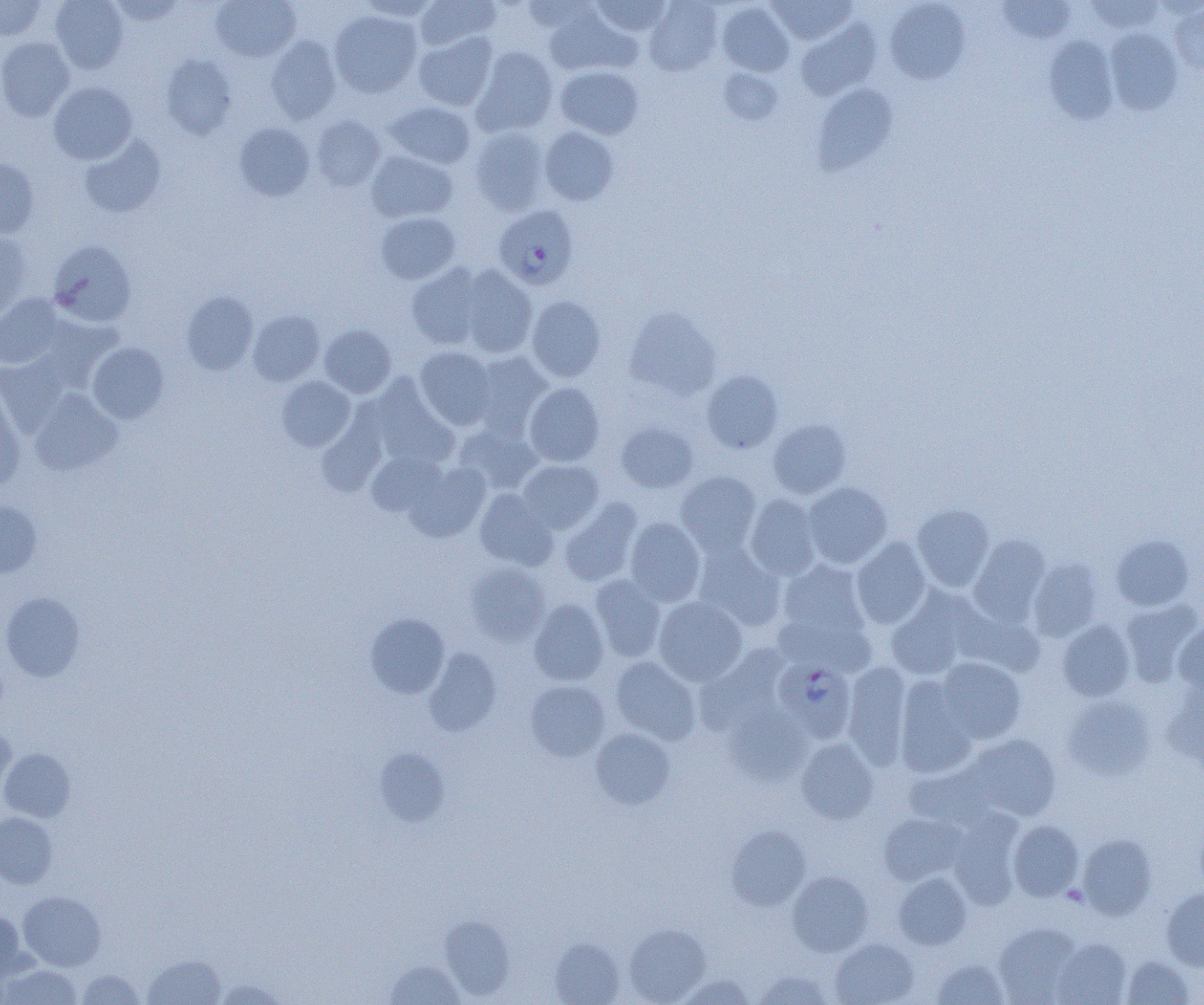

Approximate bounding boxes as named x1/y1/x2/y2 corners in pixels. Uninfected red blood cell locations: (x1=0, y1=0, x2=47, y2=40), (x1=50, y1=0, x2=128, y2=74), (x1=108, y1=0, x2=186, y2=26), (x1=210, y1=0, x2=302, y2=62), (x1=356, y1=0, x2=440, y2=22), (x1=415, y1=0, x2=500, y2=51), (x1=521, y1=0, x2=599, y2=34), (x1=590, y1=0, x2=672, y2=36), (x1=644, y1=0, x2=722, y2=75), (x1=768, y1=0, x2=857, y2=45), (x1=996, y1=0, x2=1077, y2=45), (x1=1082, y1=0, x2=1166, y2=34), (x1=885, y1=1, x2=969, y2=84), (x1=717, y1=2, x2=794, y2=77), (x1=1169, y1=3, x2=1204, y2=76), (x1=544, y1=7, x2=636, y2=76), (x1=329, y1=10, x2=422, y2=98), (x1=795, y1=19, x2=880, y2=101), (x1=1104, y1=28, x2=1183, y2=115), (x1=413, y1=32, x2=498, y2=111), (x1=266, y1=35, x2=342, y2=124), (x1=1044, y1=35, x2=1119, y2=124), (x1=0, y1=37, x2=75, y2=121), (x1=471, y1=47, x2=558, y2=136), (x1=159, y1=54, x2=237, y2=140), (x1=555, y1=66, x2=644, y2=139), (x1=718, y1=68, x2=783, y2=125), (x1=48, y1=82, x2=137, y2=164), (x1=810, y1=83, x2=900, y2=175), (x1=384, y1=102, x2=475, y2=169), (x1=311, y1=115, x2=387, y2=191), (x1=234, y1=122, x2=314, y2=201), (x1=469, y1=125, x2=551, y2=215), (x1=539, y1=126, x2=619, y2=206), (x1=79, y1=136, x2=166, y2=218), (x1=366, y1=151, x2=458, y2=222), (x1=0, y1=157, x2=40, y2=238), (x1=375, y1=211, x2=460, y2=285), (x1=0, y1=232, x2=33, y2=319), (x1=48, y1=239, x2=137, y2=327), (x1=407, y1=263, x2=487, y2=350), (x1=457, y1=265, x2=537, y2=358), (x1=181, y1=291, x2=258, y2=375), (x1=0, y1=294, x2=64, y2=369), (x1=526, y1=295, x2=606, y2=382), (x1=623, y1=307, x2=722, y2=401), (x1=247, y1=310, x2=325, y2=386), (x1=320, y1=325, x2=396, y2=398), (x1=87, y1=342, x2=169, y2=423), (x1=415, y1=347, x2=497, y2=430), (x1=471, y1=351, x2=553, y2=436), (x1=0, y1=354, x2=70, y2=436), (x1=701, y1=370, x2=783, y2=454), (x1=276, y1=376, x2=355, y2=451), (x1=368, y1=378, x2=459, y2=469), (x1=524, y1=382, x2=605, y2=466), (x1=0, y1=386, x2=24, y2=491), (x1=29, y1=389, x2=122, y2=476), (x1=316, y1=411, x2=387, y2=497), (x1=768, y1=419, x2=851, y2=498), (x1=616, y1=421, x2=697, y2=493), (x1=454, y1=424, x2=543, y2=495), (x1=366, y1=451, x2=447, y2=517), (x1=517, y1=459, x2=604, y2=534), (x1=405, y1=462, x2=490, y2=542), (x1=676, y1=471, x2=762, y2=557), (x1=802, y1=481, x2=892, y2=569), (x1=474, y1=488, x2=558, y2=571), (x1=745, y1=493, x2=822, y2=580), (x1=559, y1=497, x2=643, y2=587), (x1=0, y1=500, x2=42, y2=577), (x1=911, y1=504, x2=995, y2=592), (x1=625, y1=517, x2=705, y2=607), (x1=1110, y1=534, x2=1195, y2=611), (x1=968, y1=535, x2=1051, y2=624), (x1=851, y1=537, x2=932, y2=629), (x1=692, y1=542, x2=786, y2=631), (x1=1028, y1=557, x2=1103, y2=641), (x1=777, y1=559, x2=871, y2=645), (x1=464, y1=562, x2=552, y2=645), (x1=589, y1=574, x2=667, y2=662), (x1=886, y1=586, x2=981, y2=680), (x1=1, y1=591, x2=85, y2=681), (x1=654, y1=596, x2=747, y2=686), (x1=529, y1=598, x2=609, y2=686), (x1=1120, y1=599, x2=1202, y2=686), (x1=953, y1=602, x2=1044, y2=677), (x1=365, y1=613, x2=449, y2=698), (x1=1056, y1=619, x2=1136, y2=701), (x1=1173, y1=620, x2=1204, y2=696), (x1=696, y1=646, x2=793, y2=738), (x1=423, y1=648, x2=501, y2=737), (x1=610, y1=657, x2=701, y2=746), (x1=934, y1=657, x2=1027, y2=744), (x1=842, y1=662, x2=912, y2=769), (x1=894, y1=676, x2=980, y2=778), (x1=525, y1=680, x2=610, y2=762), (x1=1161, y1=684, x2=1204, y2=772), (x1=1061, y1=694, x2=1158, y2=781), (x1=722, y1=701, x2=811, y2=784), (x1=590, y1=727, x2=675, y2=810), (x1=0, y1=728, x2=16, y2=800), (x1=965, y1=734, x2=1061, y2=821), (x1=796, y1=737, x2=879, y2=824), (x1=375, y1=747, x2=450, y2=827), (x1=1, y1=748, x2=75, y2=821), (x1=904, y1=764, x2=999, y2=831), (x1=948, y1=810, x2=1025, y2=908), (x1=0, y1=812, x2=58, y2=888), (x1=878, y1=812, x2=967, y2=887), (x1=1008, y1=820, x2=1084, y2=901), (x1=726, y1=826, x2=811, y2=910), (x1=1077, y1=833, x2=1157, y2=920), (x1=787, y1=870, x2=873, y2=956), (x1=893, y1=872, x2=971, y2=949), (x1=1161, y1=887, x2=1204, y2=970), (x1=18, y1=890, x2=106, y2=971), (x1=0, y1=910, x2=28, y2=980), (x1=440, y1=916, x2=515, y2=1000), (x1=993, y1=922, x2=1084, y2=1004), (x1=623, y1=924, x2=711, y2=1004), (x1=1052, y1=937, x2=1132, y2=1005), (x1=549, y1=938, x2=624, y2=1005), (x1=830, y1=938, x2=918, y2=1005), (x1=143, y1=954, x2=226, y2=1004), (x1=1122, y1=955, x2=1195, y2=1005), (x1=932, y1=957, x2=1009, y2=1005), (x1=386, y1=959, x2=464, y2=1004), (x1=1, y1=963, x2=83, y2=1004), (x1=76, y1=969, x2=145, y2=1004), (x1=753, y1=970, x2=833, y2=1004), (x1=676, y1=974, x2=756, y2=1004), (x1=214, y1=978, x2=288, y2=1004). Plasmodium falciparum-infected red blood cell locations: (x1=493, y1=205, x2=578, y2=290), (x1=774, y1=659, x2=856, y2=743). Slide-level diagnosis: Plasmodium falciparum. Light microscopy. Thin blood film. Single field of view. 1000x magnification. Image is 1204×1005 pixels.